Assess this cell for malaria.
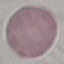
It is uninfected.

stain = Giemsa
image type = cell patch, automatically extracted from a larger field of view and resized to 64 × 64 pixels
capture = smartphone camera at the microscope eyepiece
preparation = thin blood smear